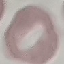

Summary:
  - Result: no malaria parasites detected
  - Stain: Giemsa
  - Preparation: thin blood film
  - Image type: cell patch, automatically extracted from a larger field of view and resized to 64 × 64 pixels
  - Capture: smartphone through the microscope eyepiece